Identify the cell.
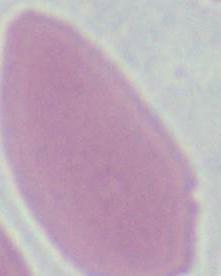

This is an erythrocyte.

{
  "modality": "photomicrograph",
  "magnification": "1000x"
}